State the blood parasite species.
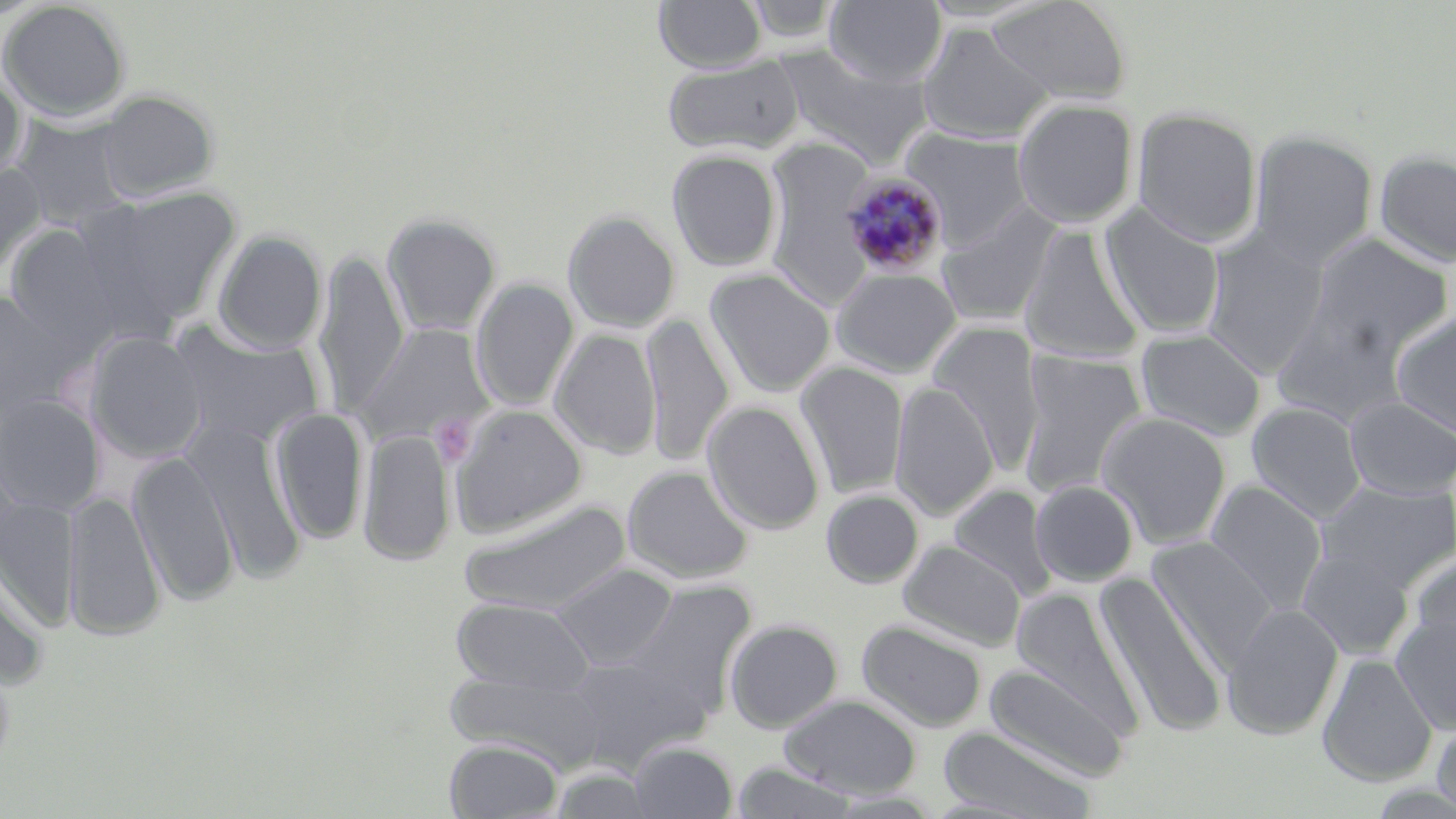

Plasmodium malariae.

preparation = thin blood film
modality = light microscopy
stain = May-Grünwald-Giemsa
magnification = 1000x
platelet locations = approximate bounding boxes as (x1,y1)-(x2,y2) corner pairs in pixels: (430,414)-(478,466)
uninfected red blood cell locations = approximate bounding boxes as (x1,y1)-(x2,y2) corner pairs in pixels: (655,0)-(766,72), (742,0)-(842,45), (824,0)-(947,86), (986,0)-(1132,104), (0,1)-(131,122), (918,24)-(1053,143), (776,51)-(933,168), (663,56)-(805,155), (0,73)-(26,180), (97,90)-(219,202), (1012,98)-(1139,228), (1131,108)-(1264,247), (12,115)-(131,228), (902,128)-(1035,250), (1249,130)-(1378,267), (764,139)-(880,310), (667,150)-(782,271), (1374,150)-(1456,268), (0,162)-(46,279), (80,187)-(242,330), (935,202)-(1063,327), (1100,205)-(1225,340), (563,210)-(681,333), (382,213)-(502,336), (1017,224)-(1146,366), (5,225)-(118,344), (1202,230)-(1330,378), (213,231)-(326,354), (1308,234)-(1452,360), (314,250)-(409,419), (830,267)-(962,377), (705,269)-(836,397), (471,278)-(579,412), (0,288)-(70,423), (1271,303)-(1409,426), (1389,310)-(1456,440), (641,314)-(733,466), (167,321)-(324,448), (927,322)-(1045,475), (356,323)-(493,450), (1135,328)-(1266,441), (551,329)-(661,459), (86,331)-(208,463), (1017,350)-(1147,499), (795,363)-(909,499), (890,381)-(999,520), (0,394)-(105,515), (1343,395)-(1456,501), (703,401)-(825,534), (1247,401)-(1367,522), (449,403)-(589,538), (271,407)-(368,544), (1097,411)-(1233,548), (186,421)-(305,581), (359,427)-(455,566), (128,450)-(240,606), (622,465)-(753,584), (1030,480)-(1139,587), (1205,480)-(1328,612), (1316,480)-(1455,593), (949,484)-(1057,600), (63,489)-(165,642), (821,490)-(923,588), (0,495)-(80,630), (461,499)-(632,614), (1148,537)-(1277,666), (898,540)-(1026,652), (1296,546)-(1415,660), (1409,554)-(1456,670), (0,556)-(49,690), (551,563)-(678,670), (1095,573)-(1230,738), (626,581)-(756,708), (1012,588)-(1143,737), (451,598)-(596,696), (1223,602)-(1344,740), (1391,611)-(1456,734), (724,619)-(843,733), (857,619)-(987,731), (1317,652)-(1437,787), (562,657)-(701,767), (984,661)-(1133,781), (445,669)-(608,770), (779,694)-(922,798), (1431,715)-(1456,819), (938,727)-(1096,818), (445,738)-(563,818), (628,742)-(738,818), (729,761)-(861,819), (549,766)-(657,818), (823,791)-(947,817)
image size = 1456×819 pixels
Plasmodium malariae-infected red blood cell locations = approximate bounding boxes as (x1,y1)-(x2,y2) corner pairs in pixels: (839,170)-(951,280)
field of view = single